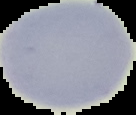
result = no malaria parasites detected
image type = segmented cell region on a black background
preparation = thin blood smear
image size = 136×115 pixels